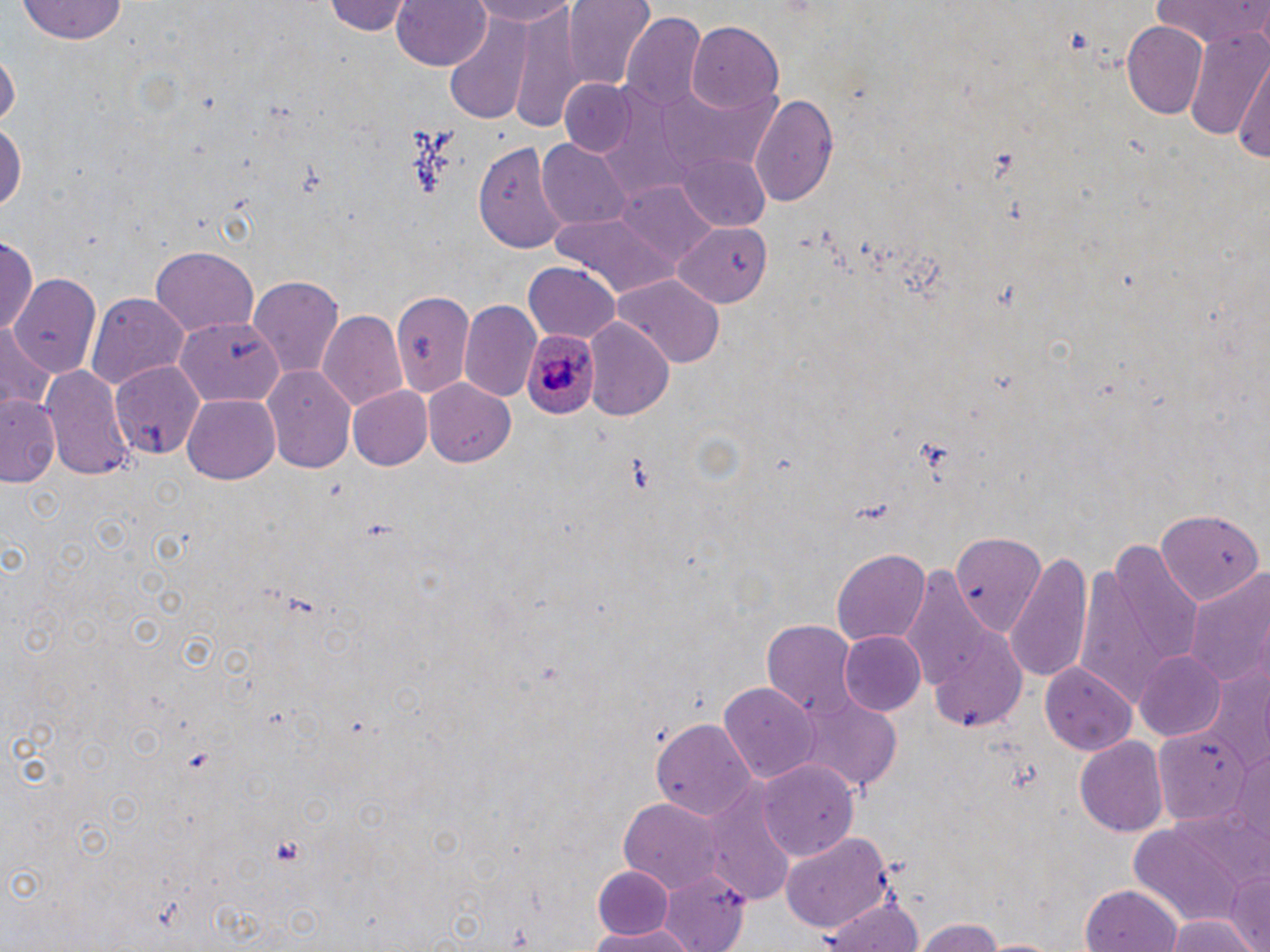

{
  "slide_level_diagnosis": "Plasmodium ovale",
  "uninfected_red_blood_cell_locations": "approximate bounding boxes as (x1, y1, x2, y2) in pixels: (325, 0, 417, 37), (390, 0, 491, 73), (466, 0, 583, 28), (564, 0, 657, 92), (1154, 0, 1270, 50), (13, 1, 134, 46), (513, 6, 582, 134), (620, 14, 708, 110), (443, 20, 535, 126), (1120, 21, 1210, 120), (688, 22, 784, 117), (1183, 23, 1270, 149), (1235, 49, 1269, 172), (1, 51, 19, 133), (558, 79, 638, 158), (751, 93, 840, 209), (0, 118, 25, 219), (537, 141, 631, 231), (474, 142, 567, 255), (677, 152, 770, 232), (545, 213, 683, 296), (672, 223, 775, 306), (2, 233, 39, 335), (151, 248, 258, 334), (523, 263, 620, 341), (249, 274, 343, 382), (9, 276, 103, 383), (616, 276, 723, 368), (393, 289, 474, 398), (85, 292, 187, 393), (458, 298, 543, 401), (317, 309, 407, 414), (175, 319, 281, 405), (587, 320, 670, 417), (0, 323, 55, 412), (109, 359, 207, 461), (43, 363, 135, 485), (264, 366, 356, 476), (423, 379, 517, 469), (345, 386, 432, 471), (181, 393, 279, 485), (1, 394, 60, 490), (1155, 509, 1261, 609), (948, 531, 1050, 631), (1078, 541, 1200, 710), (833, 547, 929, 644), (1003, 552, 1092, 685), (900, 570, 1004, 708), (1182, 570, 1270, 691), (763, 620, 858, 718), (929, 624, 1026, 732), (838, 630, 927, 717), (1134, 651, 1228, 741), (1039, 662, 1137, 753), (1197, 664, 1268, 772), (718, 679, 818, 783), (787, 697, 902, 793), (654, 719, 756, 824), (1156, 727, 1254, 826), (1073, 737, 1167, 839), (749, 757, 859, 868), (706, 787, 799, 908), (618, 797, 722, 891), (1118, 823, 1251, 941), (781, 832, 893, 936), (592, 864, 675, 939), (655, 868, 750, 951), (1226, 869, 1270, 949), (1080, 885, 1183, 952), (819, 897, 926, 952), (1166, 916, 1256, 952), (914, 918, 1012, 952), (584, 925, 702, 951)",
  "field_of_view": "single",
  "stain": "May-Grünwald-Giemsa",
  "magnification": "1000x",
  "preparation": "thin blood smear",
  "plasmodium_ovale_infected_red_blood_cell_locations": "approximate bounding boxes as (x1, y1, x2, y2) in pixels: (521, 332, 596, 416)",
  "modality": "optical microscopy",
  "platelet_locations": "approximate bounding boxes as (x1, y1, x2, y2) in pixels: (266, 833, 308, 866)",
  "image_size": "1270×952 pixels"
}